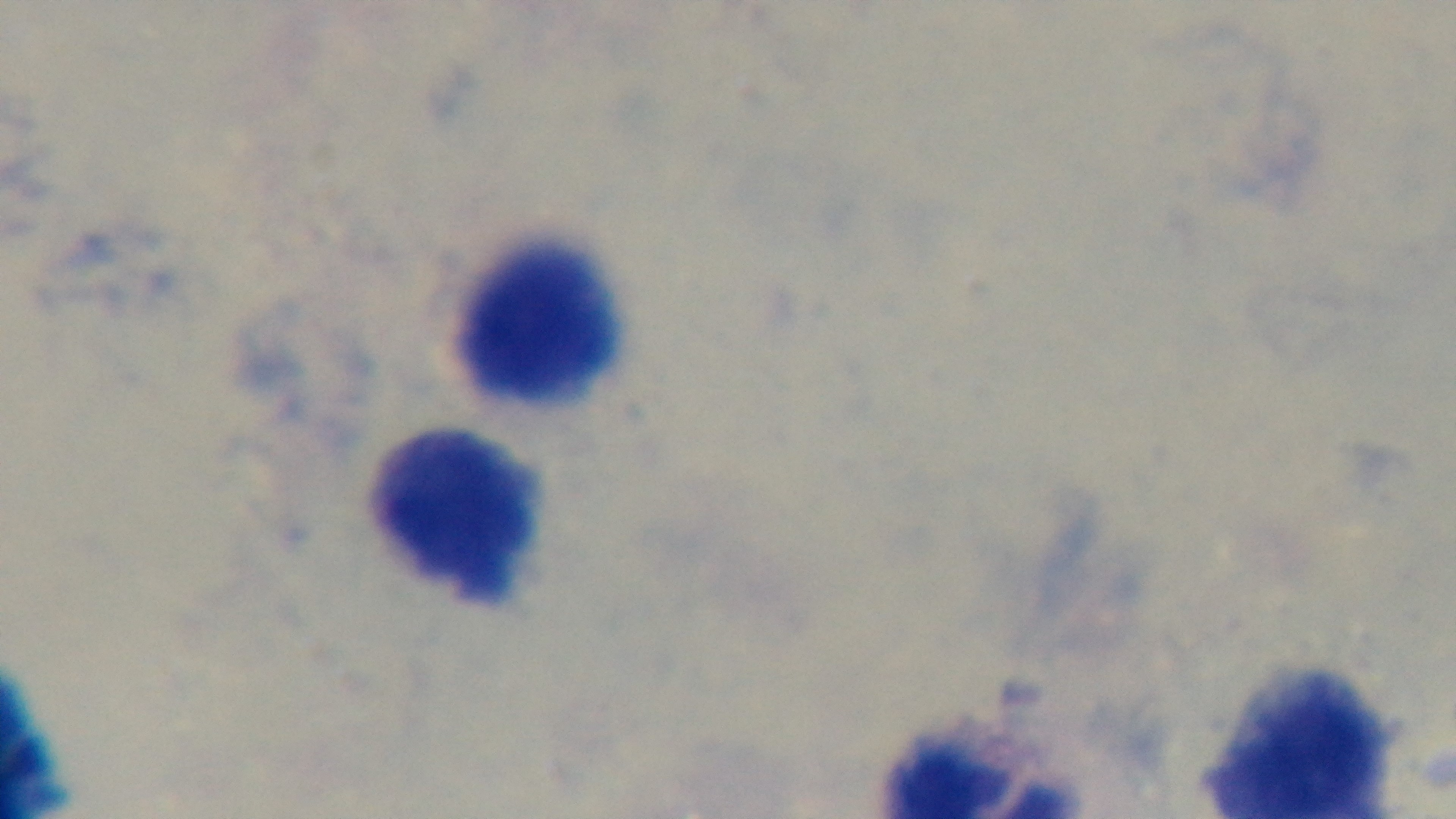
Summary:
  - Preparation: thick blood film
  - Malaria status: negative
  - Modality: light microscopy
  - Objective: 100x oil immersion
  - Stain: Giemsa
  - Field of view: one from the slide
  - Capture: mounted 4K digital camera